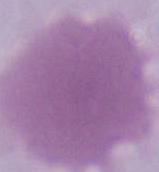
{
  "modality": "micrograph",
  "magnification": "1000x",
  "identification": "red blood cell"
}